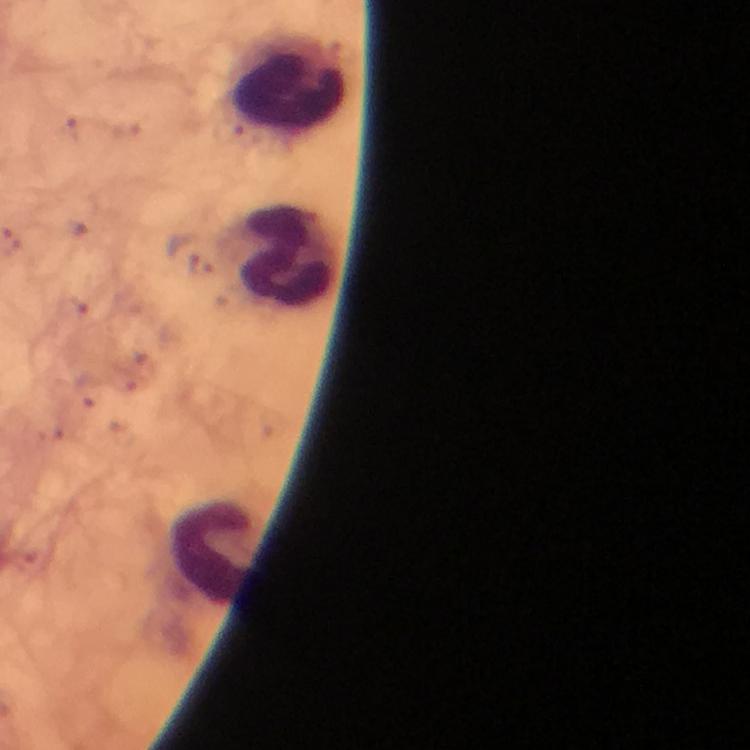

Approximate object centers, in pixels from the top-left corner.
Summary:
  - Leukocyte locations: (x=286, y=81), (x=286, y=255), (x=212, y=552)
  - Cropped from: one field of view
  - Magnification: 100x
  - Plasmodium parasites: none detected
  - Preparation: thick smear
  - Image size: 750×750 pixels
  - Capture: smartphone photograph through a microscope
  - Context: from a malaria diagnostic workup
  - Immersion oil: used
  - Stain: Giemsa